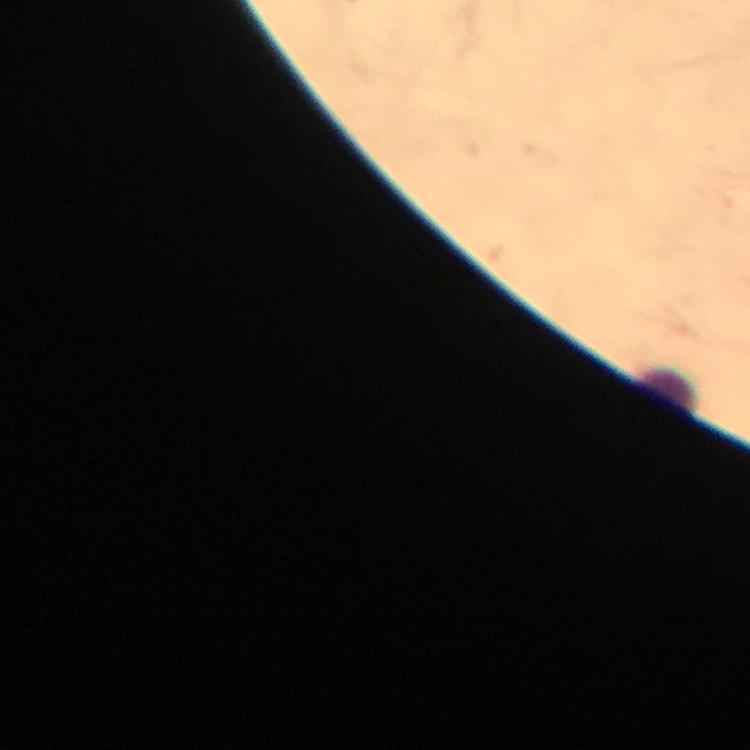

Approximate object centers, in pixels from the top-left corner.
Summary:
  - Leukocyte locations: (x=665, y=390)
  - Magnification: 100x
  - Preparation: thick smear
  - Cropped from: a single field of view
  - Image size: 750×750 pixels
  - Context: from a malaria diagnostic workup
  - Immersion oil: used
  - Capture: smartphone photograph through a microscope
  - Stain: Giemsa
  - Malaria parasites: none detected